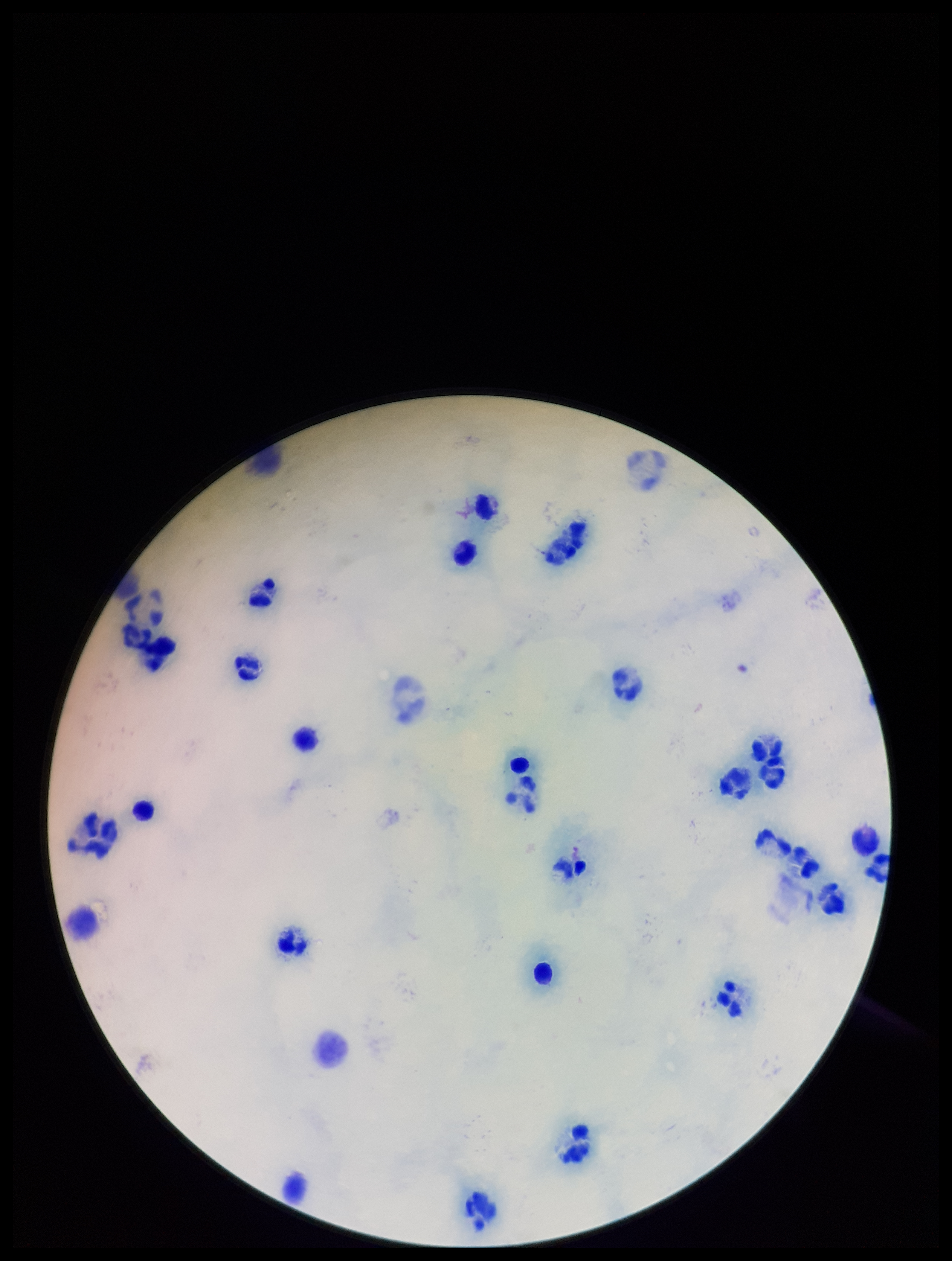

One field from this slide. Image is 952×1261 pixels. Patient malaria status: negative. Stained with Giemsa. Plasmodium parasites: none detected. Parasite count: 0. Leukocyte count: 29. Preparation: thick. Smartphone photograph taken through the eyepiece of a microscope.